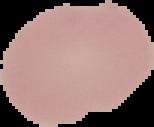
Summary:
  - Result: no malaria parasites detected
  - Image size: 154×127 pixels
  - Preparation: thin blood smear
  - Image type: segmented cell region with the area outside set to black